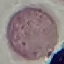
malaria status = uninfected
stain = Giemsa
preparation = thin blood smear
image type = automatically extracted cell patch, resized to 64 × 64 pixels
capture = smartphone camera at the microscope eyepiece